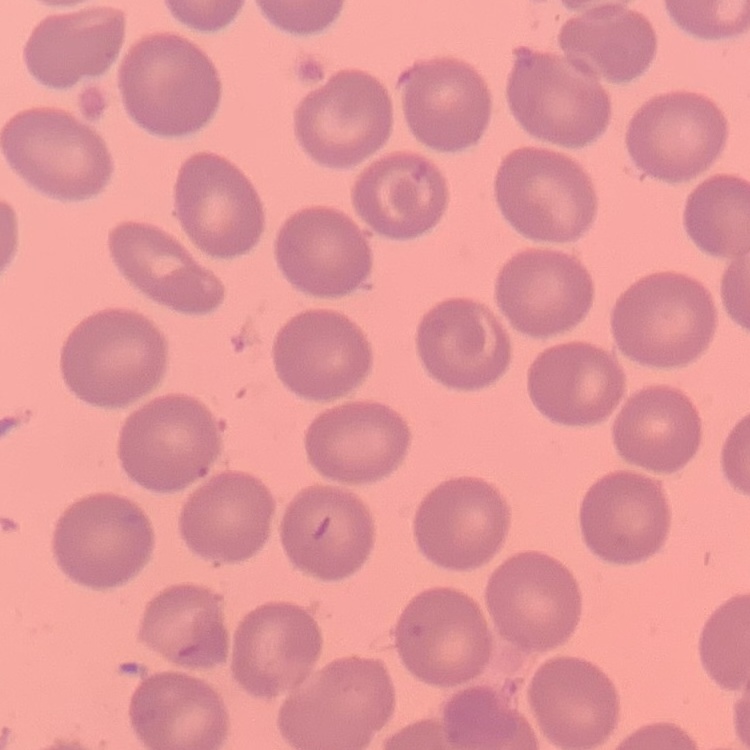
red blood cell morphology = no rouleaux formation
stain = Field's or Giemsa
preparation = thin blood film
image type = one tile cut from a larger photomicrograph